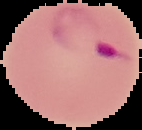
{
  "image_type": "segmented cell region with the area outside set to black",
  "image_size": "142×130 pixels",
  "result": "Plasmodium parasites identified",
  "preparation": "thin blood smear"
}